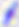

identification: Toxoplasma gondii
magnification: 400x
modality: micrograph